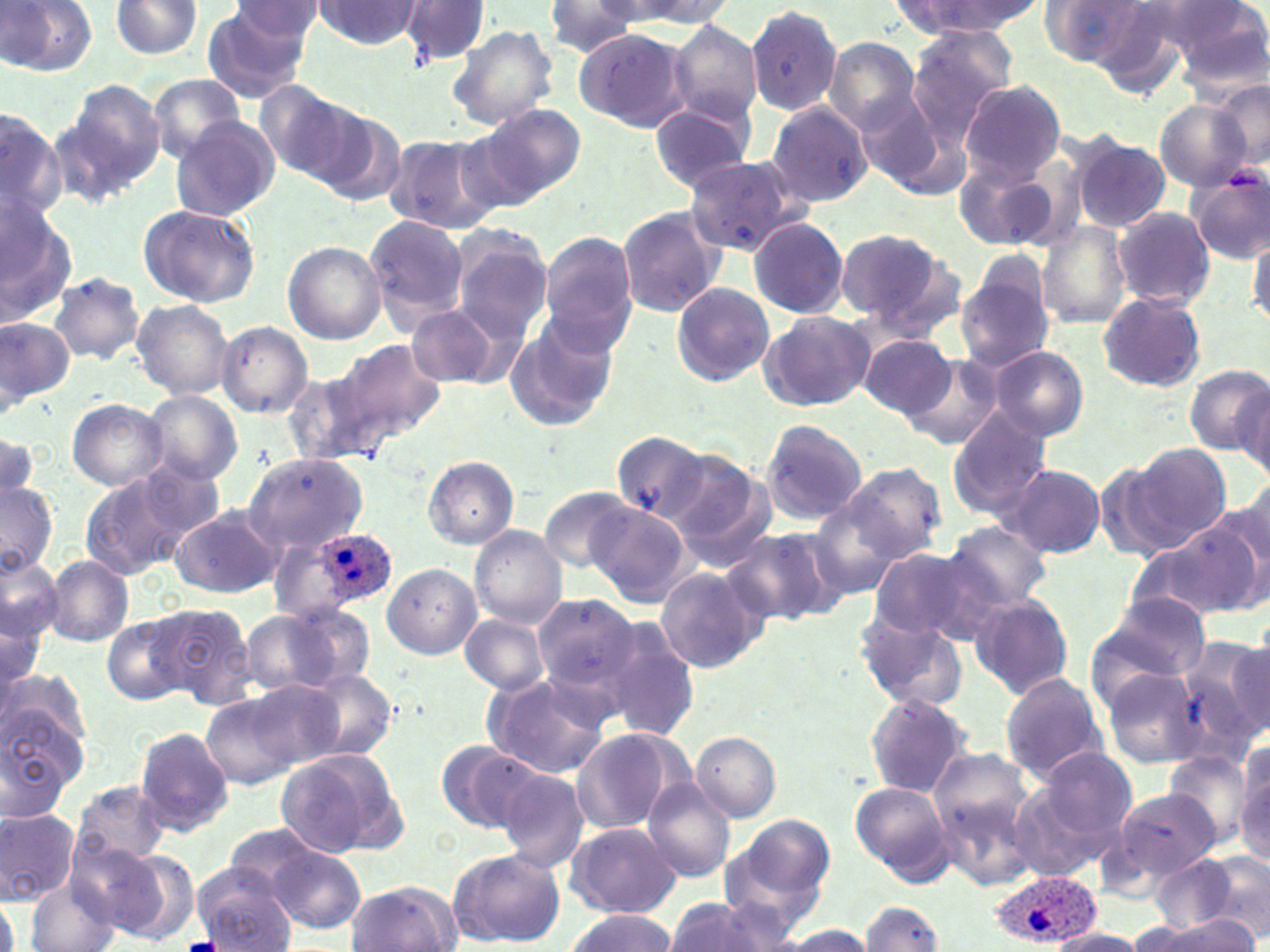
slide-level diagnosis = Plasmodium ovale
field of view = one of a larger specimen
modality = optical microscopy
stain = May-Grünwald-Giemsa
image size = 1270×952 pixels
uninfected red blood cell locations = approximate bounding boxes as (x1,y1)-(x2,y2) corner pairs in pixels: (3,0)-(97,76), (109,0)-(201,58), (400,0)-(488,65), (609,0)-(735,30), (890,0)-(1045,38), (1038,0)-(1149,68), (1171,0)-(1269,87), (310,1)-(424,51), (543,1)-(647,57), (227,2)-(327,54), (744,3)-(843,118), (201,8)-(314,103), (668,20)-(763,124), (447,23)-(559,131), (574,27)-(692,133), (907,28)-(1017,147), (823,36)-(922,133), (148,73)-(248,163), (69,80)-(166,184), (959,80)-(1067,184), (1209,80)-(1269,169), (255,81)-(363,183), (854,90)-(943,189), (767,100)-(873,206), (1154,100)-(1250,192), (479,103)-(585,202), (648,103)-(752,192), (0,107)-(66,223), (309,108)-(409,205), (170,117)-(280,221), (382,135)-(492,233), (1072,136)-(1171,232), (955,155)-(1061,250), (684,156)-(801,255), (1188,166)-(1270,262), (1,203)-(78,326), (136,203)-(260,307), (616,206)-(726,316), (1113,207)-(1215,309), (363,213)-(472,328), (746,215)-(850,320), (1038,222)-(1132,329), (448,228)-(553,345), (833,228)-(956,333), (1249,231)-(1270,329), (539,232)-(639,348), (282,241)-(386,344), (956,268)-(1055,372), (48,271)-(147,365), (671,280)-(774,387), (1095,291)-(1207,392), (131,299)-(234,398), (406,303)-(502,388), (758,310)-(876,412), (0,315)-(71,409), (504,315)-(618,431), (215,321)-(313,417), (858,334)-(957,418), (339,338)-(445,442), (989,345)-(1089,440), (901,354)-(1005,451), (1184,365)-(1269,454), (284,367)-(391,470), (1233,383)-(1269,481), (139,390)-(242,485), (66,398)-(168,491), (947,408)-(1052,518), (760,419)-(867,525), (0,430)-(41,505), (610,431)-(709,523), (1129,441)-(1234,550), (662,449)-(771,558), (243,453)-(367,555), (424,456)-(519,548), (1094,460)-(1181,563), (840,462)-(947,564), (1000,462)-(1105,560), (79,472)-(203,579), (954,477)-(1092,593), (0,481)-(57,575), (537,485)-(642,572), (1209,489)-(1270,608), (807,498)-(908,598), (589,503)-(690,605), (169,505)-(283,600), (944,521)-(1052,610), (471,525)-(566,627), (1130,525)-(1263,623), (723,526)-(839,626), (1101,539)-(1233,676), (268,543)-(339,621), (869,546)-(997,646), (0,552)-(62,647), (43,557)-(133,648), (383,563)-(481,659), (656,567)-(769,674), (531,592)-(641,700), (966,593)-(1075,699), (1091,595)-(1211,688), (148,603)-(257,708), (245,605)-(370,695), (854,610)-(970,710), (0,611)-(42,707), (509,611)-(634,755), (102,613)-(190,703), (460,615)-(550,697), (602,621)-(702,743), (1184,633)-(1270,747), (1099,666)-(1208,770), (300,667)-(398,762), (481,672)-(610,778), (998,672)-(1107,782), (245,677)-(349,771), (198,688)-(312,786), (863,692)-(975,799), (0,695)-(89,811), (133,726)-(232,835), (570,728)-(687,835), (691,731)-(780,821), (437,741)-(541,832), (1166,744)-(1256,849), (927,746)-(1041,868), (1036,746)-(1137,839), (275,748)-(407,860), (1234,748)-(1270,862), (495,765)-(591,875), (642,779)-(736,882), (1005,779)-(1118,883), (849,780)-(955,885), (71,781)-(169,868), (1112,788)-(1218,880), (0,808)-(81,904), (721,818)-(835,934), (566,821)-(680,918), (220,824)-(331,903), (267,845)-(366,932), (96,846)-(199,945), (447,848)-(565,948), (1192,850)-(1270,939), (1151,856)-(1240,932), (194,869)-(294,952), (346,880)-(464,952), (25,881)-(121,952), (0,894)-(21,952), (663,897)-(792,952), (860,901)-(943,951), (562,909)-(676,951), (1137,914)-(1254,951), (777,924)-(879,950), (1043,928)-(1148,952)
preparation = thin blood film
magnification = 1000x
Plasmodium ovale-infected red blood cell locations = approximate bounding boxes as (x1,y1)-(x2,y2) corner pairs in pixels: (309,525)-(394,606), (987,869)-(1097,947)